Point out each Plasmodium parasite.
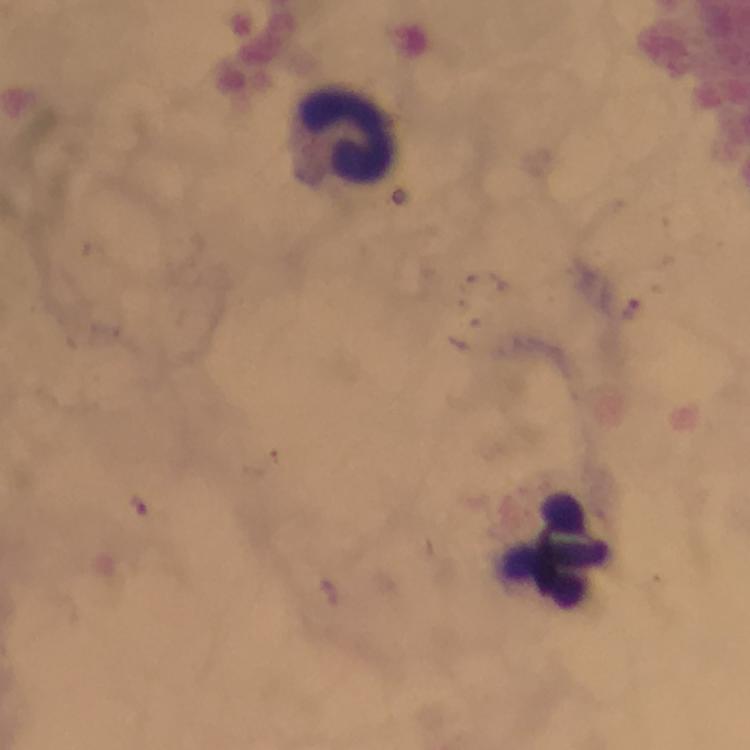
Approximate centers as [x, y] in pixels.
Plasmodium parasites: [630, 306].

Leukocyte locations: [345, 136], [559, 550]. Immersion oil was used. A crop from one field of view. Photographed with a smartphone mounted on the microscope. At 100x magnification. Giemsa-stained preparation. From a malaria diagnostic workup. Image is 750×750 pixels. Thick blood smear.